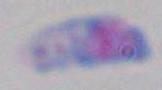
Summary:
  - Identification: Toxoplasma gondii
  - Modality: micrograph
  - Magnification: 1000x